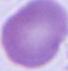 Photomicrograph. Captured at 1000x magnification. An erythrocyte is shown.